Name the parasite shown.
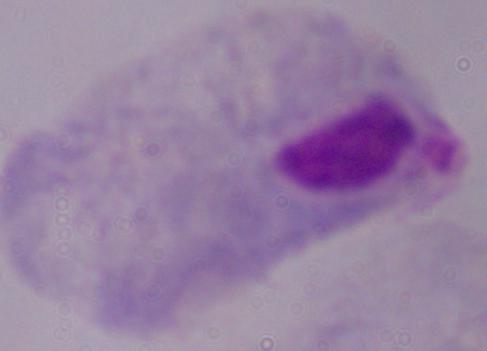
This is a trichomonad.

Summary:
  - Modality: photomicrograph
  - Magnification: 1000x